Assess this cell for malaria.
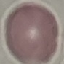
It is uninfected.

Giemsa stain. Cell patch, automatically extracted from a larger field of view and resized to 64 × 64 pixels. Acquired by smartphone through the microscope eyepiece. Thin blood smear.